Name the parasite shown.
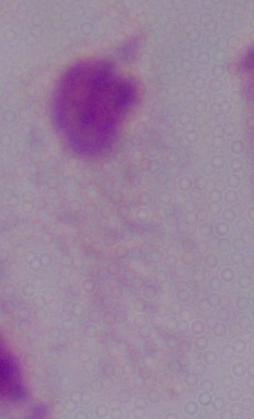
A trichomonad.

{
  "magnification": "1000x",
  "modality": "photomicrograph"
}